Identify the cell.
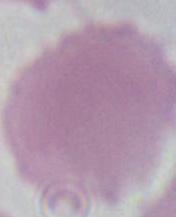
An erythrocyte.

Captured at 1000x magnification. Micrograph.